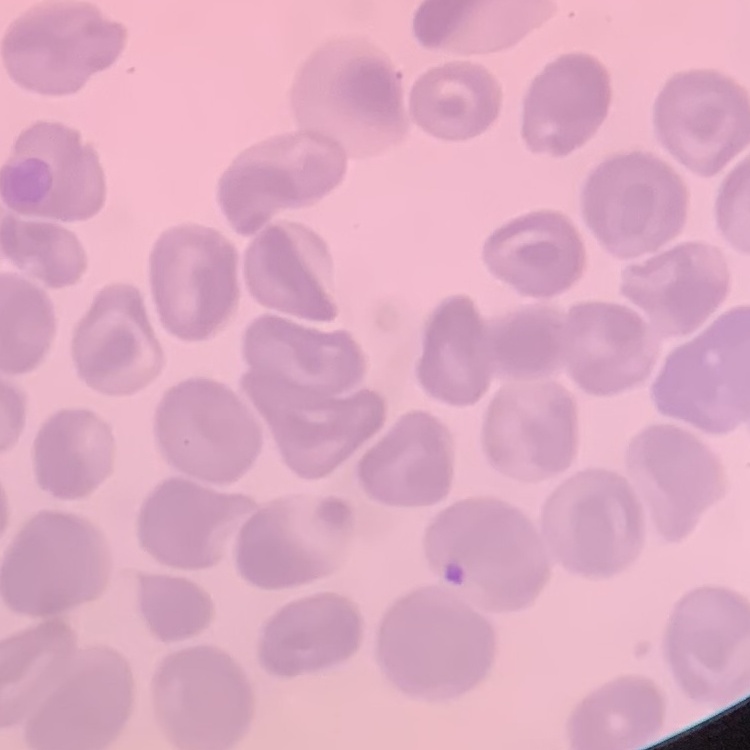
{
  "red_blood_cell_morphology": "no rouleaux formation",
  "stain": "Field's or Giemsa",
  "preparation": "thin peripheral smear",
  "image_type": "square crop of a larger photomicrograph"
}